Report the malaria status of this cell.
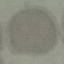

It is uninfected.

Photographed with a smartphone camera at the microscope eyepiece. Automatically extracted cell patch, resized to 64 × 64 pixels. Giemsa-stained preparation. Thin smear of blood.